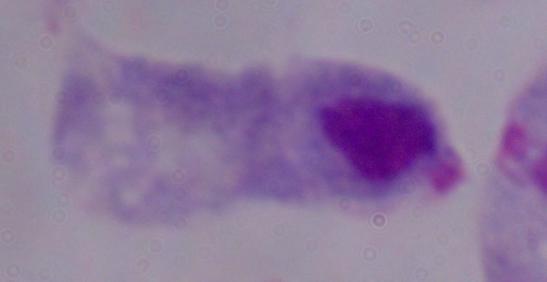
Photomicrograph. Captured at 1000x magnification. A trichomonad is seen.